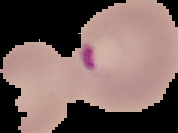 Image is 178×133 pixels. Malaria status: parasitized. From a thin blood smear. Cell region segmented out of the field of view; the surrounding area is masked to black.